Give the position of every leukocyte visible.
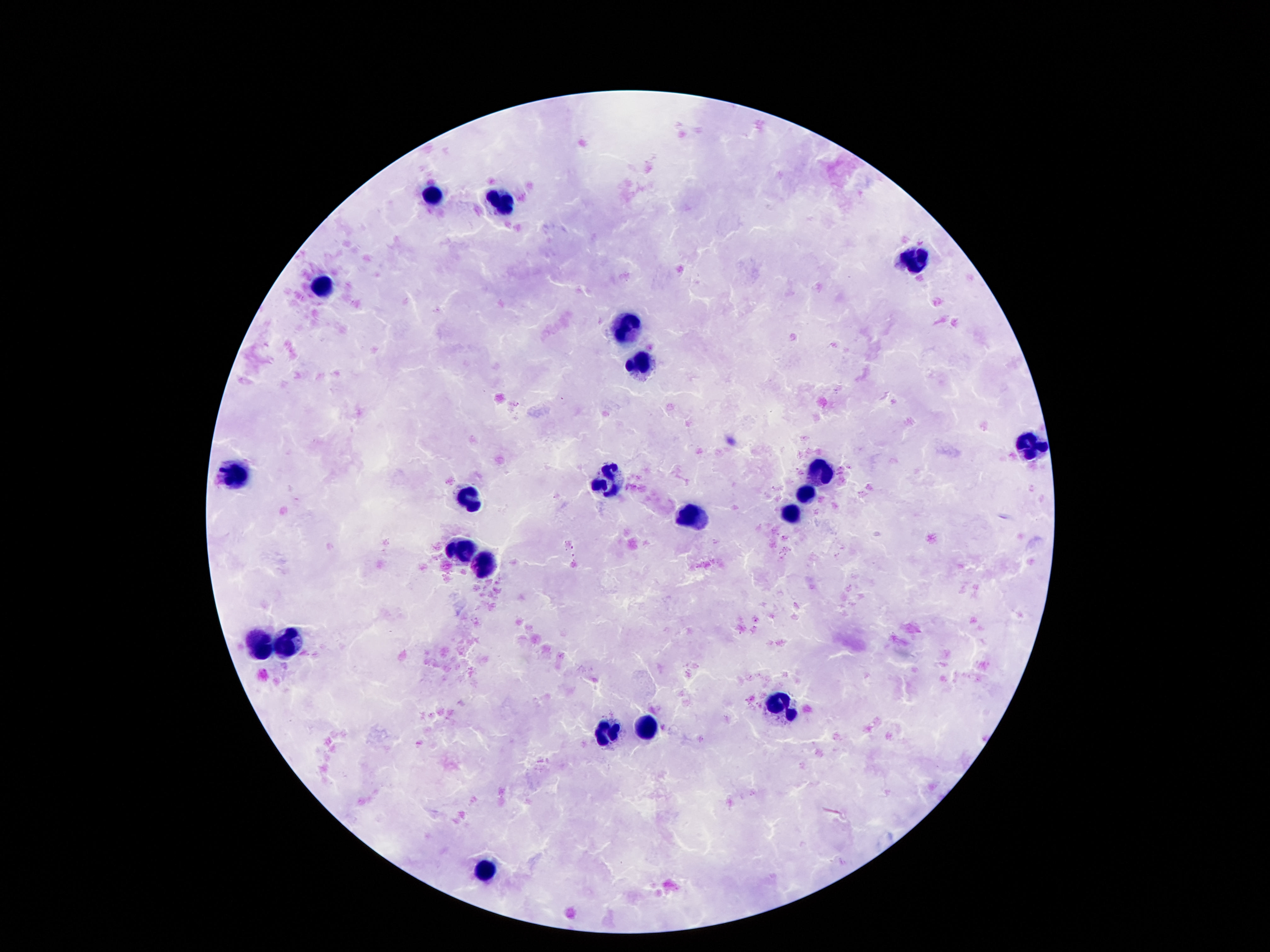

Approximate centers as (x, y) in pixels.
Leukocytes: (435, 194), (504, 204), (917, 262), (324, 282), (629, 327), (643, 364), (1027, 444), (820, 472), (233, 479), (607, 479), (808, 493), (471, 498), (794, 513), (693, 517), (463, 548), (483, 567), (262, 640), (285, 640), (777, 704), (646, 731), (610, 732), (487, 867).

{
  "patient_malaria_status": "not infected",
  "stain": "Giemsa",
  "magnification": "100x",
  "field_of_view": "single",
  "preparation": "thick peripheral-blood smear",
  "image_size": "1270×952 pixels",
  "capture": "smartphone camera through the microscope eyepiece"
}